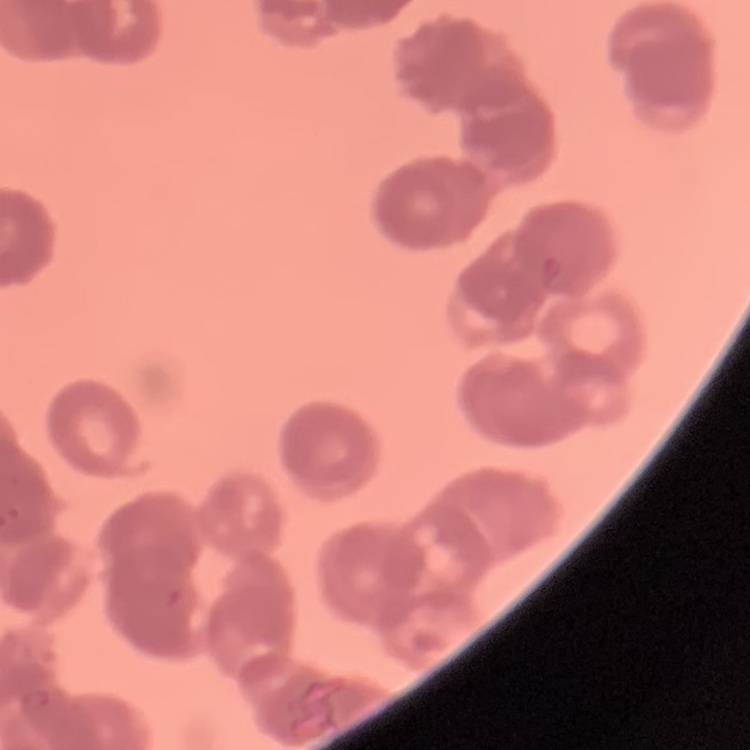

Summary:
  - Erythrocyte morphology: rouleaux formation
  - Image type: one tile cut from a larger photomicrograph
  - Preparation: thin blood smear
  - Stain: Field's or Giemsa